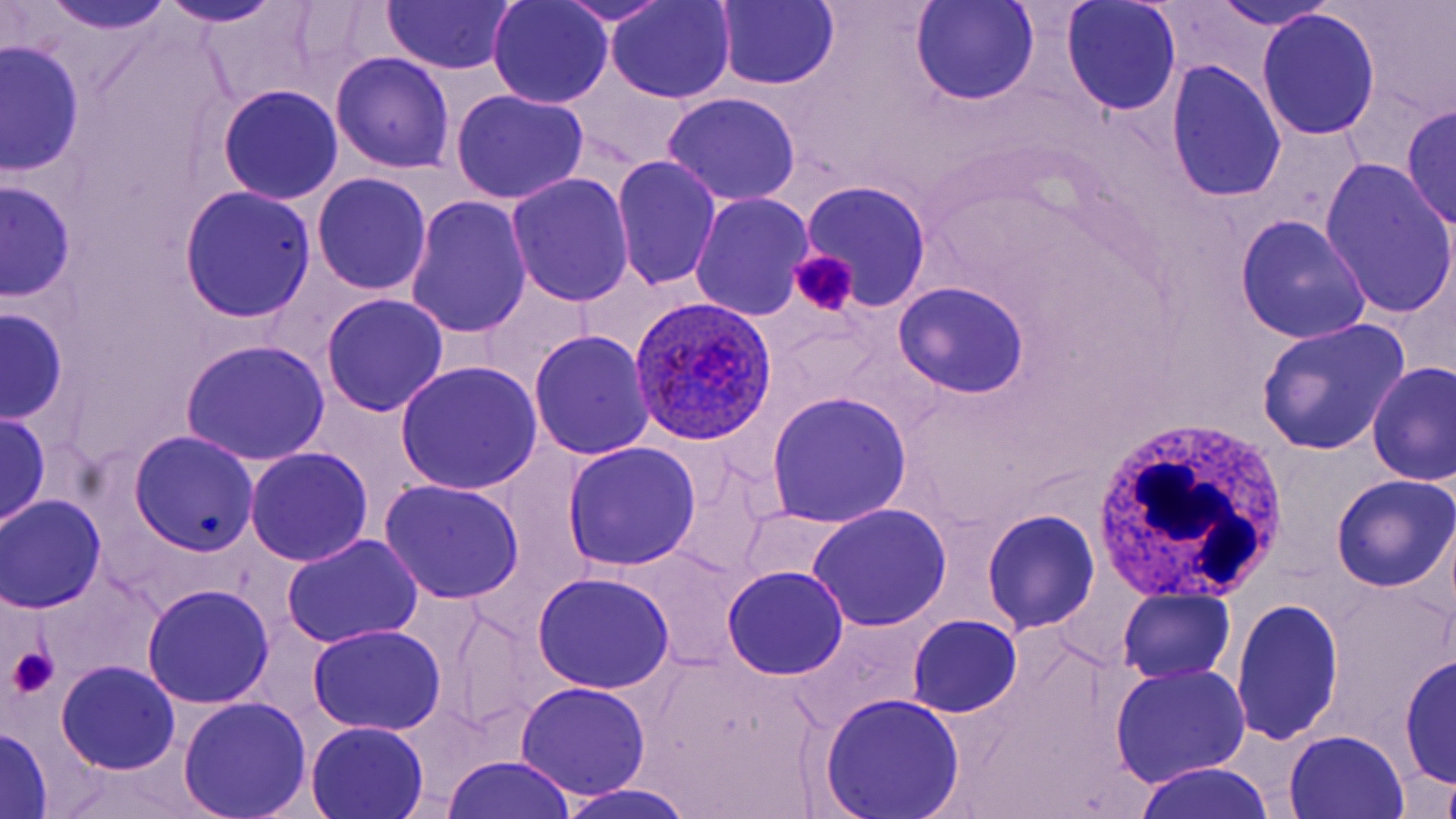
Summary:
  - Coordinate format: approximate bounding boxes as (x1,y1)-(x2,y2) corner pairs in pixels
  - Plasmodium ovale-infected red blood cell locations: (630,294)-(782,444)
  - Uninfected red blood cell locations: (23,0)-(179,38), (381,0)-(517,74), (1210,0)-(1337,30), (911,1)-(1040,106), (156,2)-(292,28), (487,2)-(613,109), (551,2)-(678,26), (607,2)-(734,103), (714,2)-(841,90), (1062,2)-(1181,116), (1256,10)-(1381,143), (2,39)-(84,180), (330,52)-(456,174), (1167,62)-(1287,201), (217,85)-(344,204), (450,89)-(589,205), (661,91)-(803,207), (1401,103)-(1456,230), (612,156)-(722,293), (1320,160)-(1456,319), (313,173)-(431,296), (506,173)-(635,306), (1,179)-(77,301), (801,182)-(932,310), (179,187)-(317,323), (690,192)-(813,321), (406,197)-(533,340), (1234,215)-(1372,344), (892,282)-(1031,400), (321,293)-(450,417), (1,307)-(68,425), (774,313)-(881,410), (1255,318)-(1411,455), (528,332)-(654,462), (180,339)-(330,466), (394,361)-(543,494), (1367,361)-(1456,486), (766,391)-(913,528), (0,411)-(50,531), (128,431)-(258,556), (562,442)-(701,571), (245,448)-(372,567), (665,462)-(773,581), (1332,474)-(1456,592), (378,480)-(525,604), (0,495)-(105,614), (807,504)-(954,628), (981,509)-(1100,635), (282,535)-(424,649), (722,565)-(850,679), (531,572)-(677,694), (45,575)-(160,688), (142,584)-(274,709), (1117,590)-(1236,684), (1231,598)-(1345,744), (448,610)-(545,730), (909,615)-(1023,718), (307,623)-(447,736), (1400,651)-(1455,792), (56,661)-(181,774), (1108,663)-(1252,788), (515,681)-(652,800), (818,693)-(967,819), (176,698)-(311,819), (304,721)-(429,818), (0,727)-(53,817), (1284,733)-(1407,818), (441,753)-(580,818), (1130,762)-(1279,819), (49,764)-(214,819), (1440,773)-(1456,819), (554,782)-(698,819)
  - White blood cell locations: (1087,414)-(1293,609)
  - Platelet locations: (789,248)-(858,318), (7,646)-(60,698)
  - Slide-level diagnosis: Plasmodium ovale
  - Modality: light microscopy
  - Magnification: 1000x
  - Preparation: thin blood film
  - Stain: May-Grünwald-Giemsa
  - Image size: 1456×819 pixels
  - Field of view: one of a larger specimen